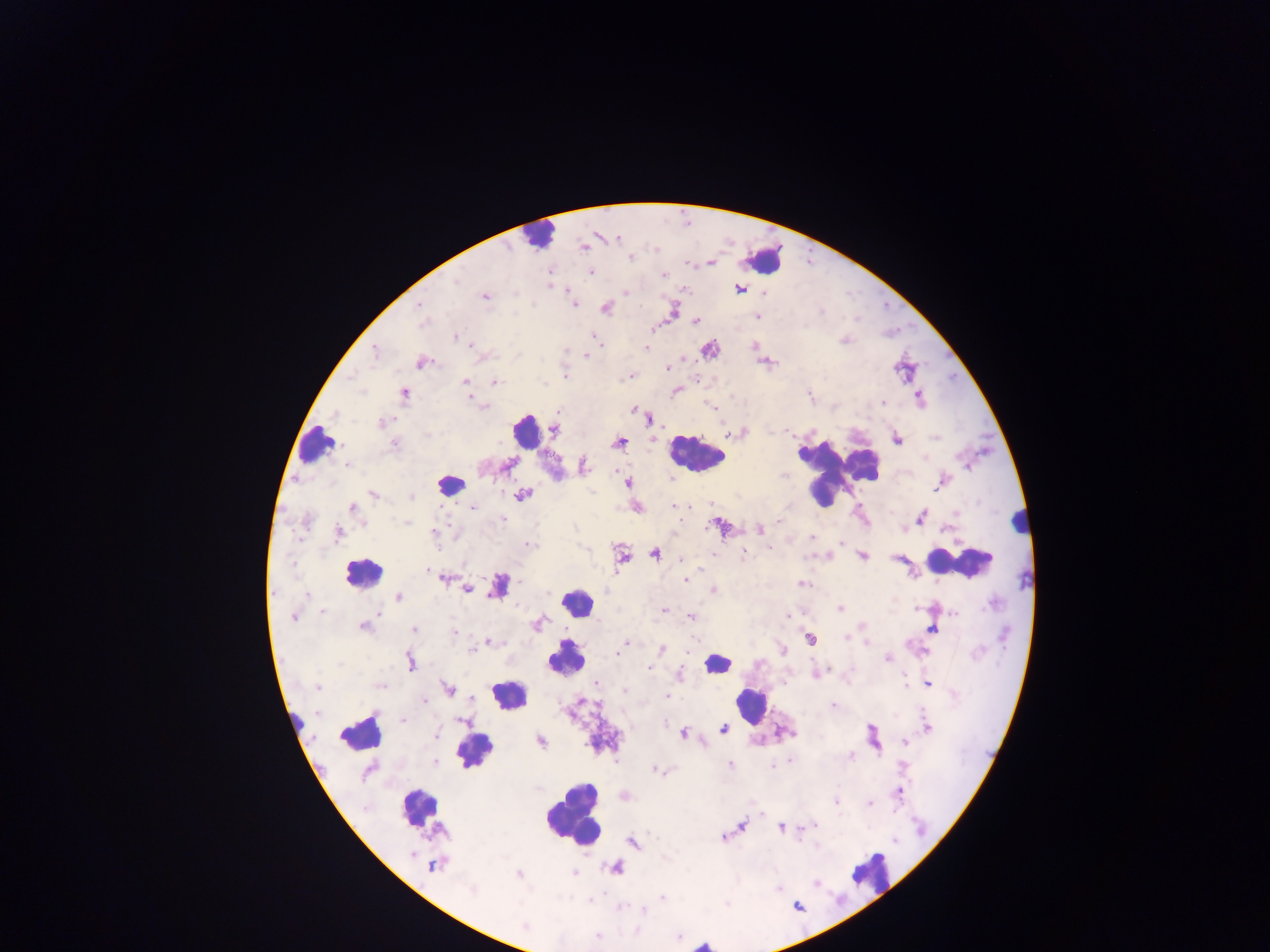

malaria_parasite_locations: 'approximate centers as (x, y) in pixels: (617, 238), (584, 247), (631, 257), (710, 263), (590, 272), (663, 275), (457, 280), (740, 290), (626, 292), (763, 292), (484, 296), (419, 304), (573, 304), (605, 308), (421, 316), (757, 317), (696, 322), (422, 323), (456, 337), (594, 338), (599, 343), (473, 346), (646, 348), (374, 352), (586, 355), (420, 363), (667, 368), (565, 376), (465, 382), (495, 382), (363, 391), (405, 394), (918, 395), (883, 402), (483, 406), (633, 410), (558, 411), (649, 421), (383, 422), (554, 431), (739, 432), (427, 435), (897, 439), (620, 442), (395, 445), (507, 465), (584, 465), (346, 466), (627, 483), (936, 487), (373, 494), (522, 495), (411, 497), (674, 506), (473, 507), (685, 507), (352, 508), (921, 517), (502, 520), (778, 521), (407, 523), (364, 525), (759, 529), (338, 533), (434, 533), (812, 537), (530, 545), (769, 549), (743, 551), (654, 554), (712, 554), (862, 556), (682, 560), (427, 572), (442, 578), (685, 580), (802, 584), (466, 589), (713, 590), (306, 594), (399, 596), (840, 608), (664, 610), (322, 611), (954, 613), (378, 614), (787, 616), (691, 617), (293, 618), (538, 623), (363, 627), (932, 629), (413, 630), (454, 632), (847, 638), (810, 640), (488, 642), (625, 644), (866, 644), (662, 649), (782, 650), (470, 651), (617, 654), (887, 659), (410, 661), (339, 664), (649, 668), (830, 669), (905, 678), (596, 683), (928, 683), (380, 686), (317, 687), (447, 689), (625, 691), (666, 695), (472, 699), (425, 701), (833, 705), (316, 714), (403, 720), (463, 722), (928, 727), (723, 729), (724, 729), (683, 733), (436, 736), (541, 741), (905, 741), (852, 756), (791, 760), (435, 762), (730, 764), (773, 766), (902, 766), (655, 770), (368, 771), (899, 793), (835, 802), (869, 803), (816, 824), (742, 826), (782, 828), (725, 838), (895, 841), (633, 843), (411, 853), (433, 865), (519, 873), (574, 874), (816, 883), (471, 891), (662, 898), (644, 911), (525, 926), (599, 935)'
preparation: thick blood smear
capture: mobile-phone photograph through a microscope
image_size: 1270×952 pixels
field_of_view: single
country: Ghana
leukocyte_locations: 'approximate centers as (x, y) in pixels: (537, 237), (764, 260), (526, 431), (316, 444), (695, 457), (824, 473), (451, 483), (1018, 519), (960, 562), (363, 572), (576, 601), (567, 659), (717, 664), (507, 694), (750, 705), (359, 733), (474, 745), (419, 807), (574, 814), (867, 872)'